Assess this cell for malaria.
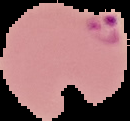
Parasitized.

Summary:
  - Image type: cell region segmented out of the field of view; surrounding area masked to black
  - Image size: 130×121 pixels
  - Preparation: thin blood film